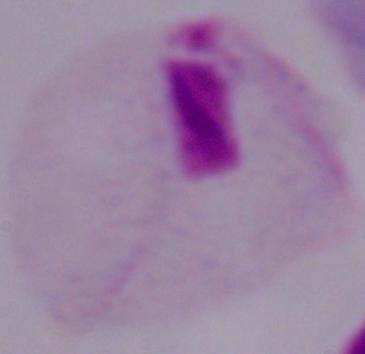
Photomicrograph. A trichomonad is shown. Captured at 1000x magnification.